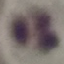

Summary:
  - Result: no malaria parasites seen
  - Image type: automatically extracted cell patch, resized to 64 × 64 pixels
  - Capture: smartphone camera at the microscope eyepiece
  - Stain: Giemsa
  - Preparation: thin blood film